Identify the parasite.
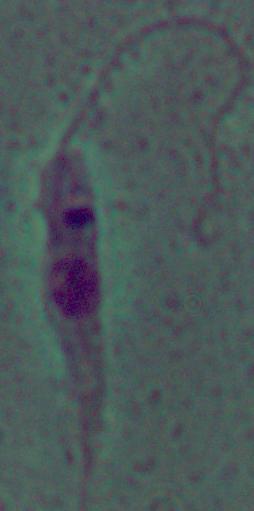
This is Leishmania.

Summary:
  - Modality: photomicrograph
  - Magnification: 1000x